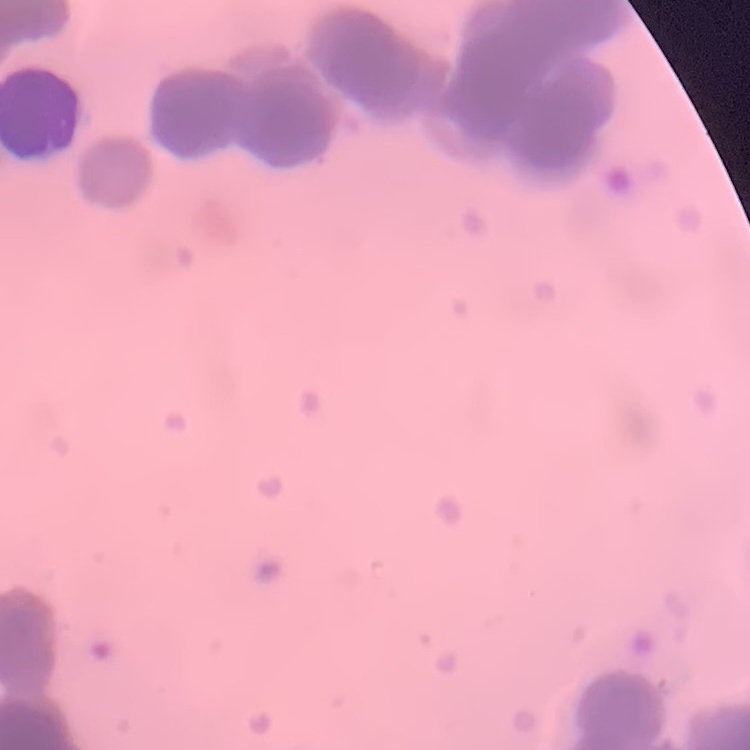 The erythrocytes exhibit rouleaux formation. Square crop of a larger photomicrograph. Thin blood smear. Stained with either Field's or Giemsa.